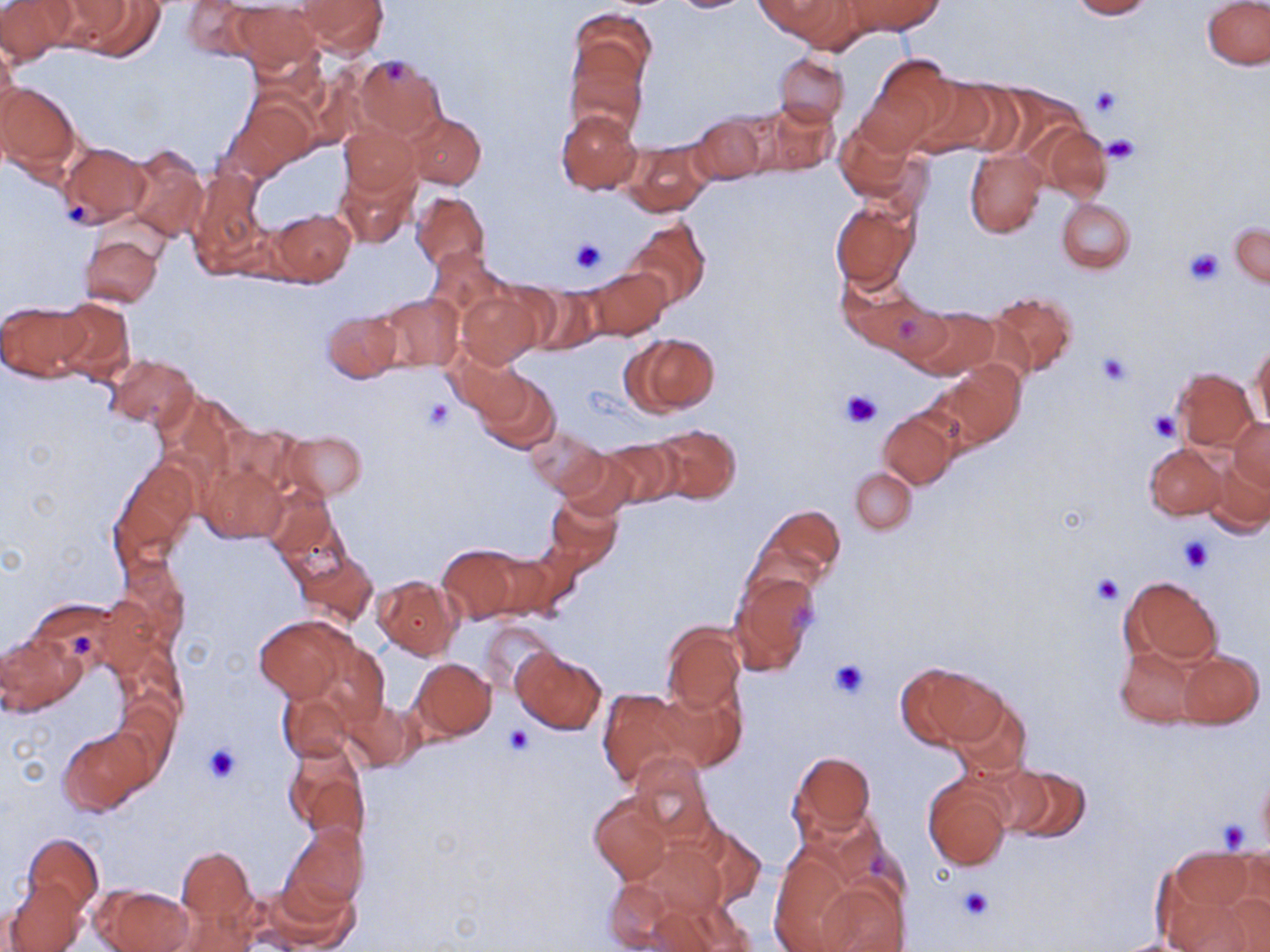
slide-level diagnosis = negative for blood parasites
uninfected red blood cell locations = approximate bounding boxes as [x1, y1, x2, y2] in pixels: [0, 0, 72, 64], [670, 0, 752, 13], [777, 0, 874, 53], [844, 0, 942, 35], [1070, 0, 1153, 19], [59, 1, 163, 59], [180, 1, 254, 58], [1202, 1, 1270, 70], [297, 2, 390, 55], [230, 3, 322, 71], [569, 8, 654, 95], [1, 41, 20, 125], [566, 49, 647, 138], [773, 53, 849, 127], [868, 53, 958, 145], [354, 55, 446, 139], [910, 77, 1006, 156], [0, 81, 80, 174], [233, 100, 315, 176], [743, 100, 837, 179], [555, 108, 642, 195], [404, 112, 485, 189], [686, 114, 769, 187], [835, 118, 923, 206], [339, 123, 420, 202], [1036, 123, 1113, 203], [622, 141, 712, 215], [58, 143, 149, 227], [125, 144, 209, 241], [965, 149, 1047, 237], [334, 161, 420, 249], [187, 168, 266, 274], [411, 190, 490, 273], [1056, 196, 1136, 273], [830, 203, 918, 290], [268, 209, 355, 285], [626, 217, 710, 310], [1230, 221, 1270, 289], [80, 234, 164, 308], [426, 248, 511, 327], [588, 267, 671, 339], [845, 283, 945, 364], [530, 287, 602, 356], [457, 288, 543, 369], [987, 291, 1078, 379], [372, 292, 463, 374], [50, 297, 134, 383], [1, 300, 87, 382], [911, 308, 997, 378], [323, 310, 402, 382], [623, 333, 720, 416], [1250, 342, 1270, 431], [106, 353, 198, 430], [454, 354, 542, 437], [936, 363, 1025, 447], [1172, 368, 1258, 449], [476, 371, 560, 453], [879, 411, 958, 488], [1230, 417, 1270, 492], [647, 423, 741, 506], [526, 427, 608, 497], [284, 430, 366, 500], [599, 439, 681, 508], [1145, 443, 1226, 519], [555, 448, 636, 519], [1203, 450, 1270, 535], [110, 460, 200, 572], [199, 460, 285, 545], [849, 468, 916, 534], [264, 484, 340, 568], [544, 494, 622, 570], [755, 503, 846, 589], [438, 545, 526, 621], [297, 551, 377, 627], [729, 572, 820, 675], [1118, 574, 1222, 671], [373, 575, 461, 659], [253, 615, 353, 703], [480, 620, 558, 694], [662, 622, 746, 711], [0, 630, 83, 715], [1114, 641, 1211, 728], [513, 648, 606, 734], [1173, 649, 1264, 729], [411, 658, 496, 740], [898, 662, 1005, 748], [657, 682, 747, 772], [278, 687, 355, 763], [596, 687, 694, 788], [948, 693, 1033, 781], [339, 697, 423, 772], [59, 727, 150, 814], [283, 742, 370, 844], [790, 751, 876, 838], [628, 753, 716, 844], [993, 760, 1094, 844], [1256, 768, 1270, 854], [924, 775, 1013, 871], [590, 795, 672, 884], [281, 822, 368, 913], [691, 824, 768, 908], [24, 833, 102, 914], [631, 839, 739, 924], [769, 843, 872, 952], [178, 848, 254, 923], [1156, 849, 1262, 952], [805, 872, 910, 952], [600, 874, 710, 949], [4, 877, 87, 952], [256, 878, 361, 950], [97, 884, 193, 952], [649, 895, 756, 952], [1104, 936, 1211, 952]
magnification = 1000x
modality = light microscopy
preparation = thin blood smear
stain = May-Grünwald-Giemsa
platelet locations = approximate bounding boxes as [x1, y1, x2, y2] in pixels: [1092, 86, 1123, 117], [1104, 134, 1142, 164], [64, 200, 91, 225], [570, 237, 608, 276], [1183, 248, 1225, 285], [1096, 351, 1132, 387], [842, 389, 881, 428], [425, 398, 454, 431], [1148, 410, 1180, 442], [1179, 537, 1211, 573], [1091, 574, 1125, 605], [71, 633, 93, 657], [830, 659, 872, 698], [505, 726, 534, 756], [204, 743, 242, 784], [1217, 819, 1252, 852], [956, 886, 993, 921]
field of view = single
image size = 1270×952 pixels